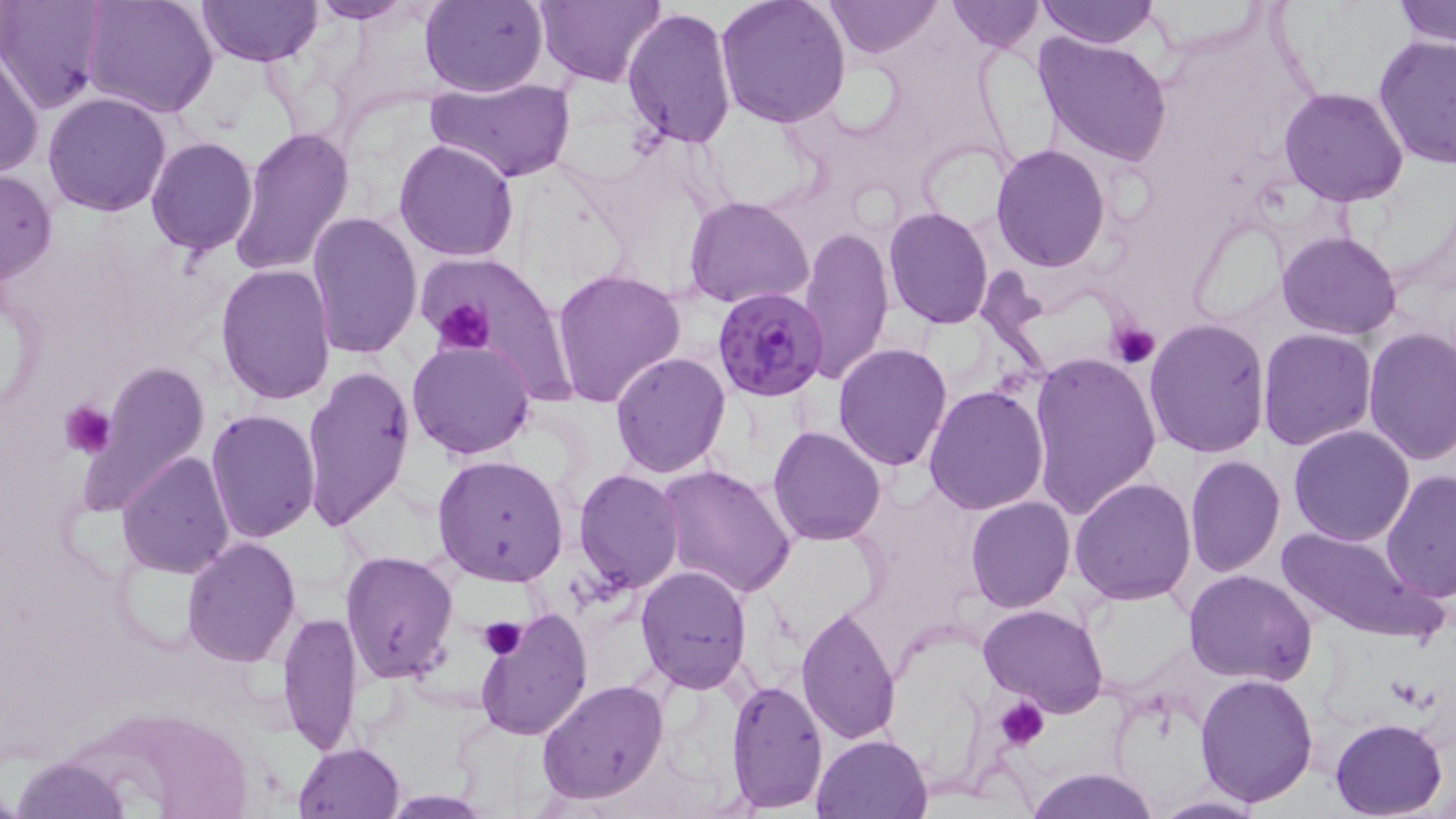
Summary:
  - Coordinate format: approximate bounding boxes as [x1, y1, x2, y2] in pixels
  - Uninfected red blood cell locations: [0, 0, 107, 112], [81, 0, 219, 118], [194, 0, 325, 67], [306, 0, 418, 22], [419, 0, 548, 98], [537, 0, 662, 87], [715, 0, 852, 128], [822, 0, 942, 57], [944, 0, 1045, 53], [1037, 0, 1160, 48], [1398, 0, 1456, 48], [622, 6, 737, 149], [1034, 31, 1172, 167], [1373, 34, 1456, 169], [0, 49, 44, 179], [427, 77, 573, 184], [1278, 87, 1409, 208], [43, 91, 171, 217], [229, 125, 354, 275], [145, 135, 259, 255], [394, 137, 521, 261], [991, 143, 1111, 270], [0, 169, 58, 287], [686, 196, 814, 310], [883, 208, 994, 330], [305, 210, 423, 359], [800, 225, 893, 383], [1278, 232, 1402, 340], [215, 263, 336, 406], [551, 268, 687, 407], [3, 279, 47, 419], [1143, 317, 1271, 458], [1258, 327, 1376, 449], [1362, 328, 1456, 466], [406, 338, 536, 461], [833, 343, 956, 469], [1027, 349, 1162, 517], [609, 351, 730, 476], [82, 358, 211, 512], [302, 362, 416, 533], [923, 384, 1051, 516], [205, 407, 320, 543], [767, 426, 887, 547], [1288, 426, 1415, 547], [117, 450, 236, 578], [432, 454, 569, 587], [1185, 454, 1285, 578], [656, 463, 798, 599], [574, 468, 683, 594], [1380, 471, 1456, 600], [1069, 478, 1197, 606], [964, 496, 1075, 613], [1276, 526, 1438, 644], [181, 536, 302, 666], [340, 550, 459, 685], [636, 567, 753, 694], [1183, 568, 1316, 684], [796, 603, 900, 745], [978, 603, 1109, 717], [278, 609, 366, 755], [474, 610, 593, 739], [1194, 672, 1318, 806], [536, 679, 669, 804], [727, 680, 827, 808], [1328, 717, 1448, 819], [811, 733, 932, 818], [293, 741, 405, 819], [10, 753, 130, 819], [1026, 767, 1160, 819], [1147, 795, 1266, 818]
  - Platelet locations: [428, 297, 496, 357], [1108, 320, 1161, 368], [59, 399, 116, 460], [478, 618, 528, 660], [996, 697, 1050, 749]
  - Plasmodium falciparum-infected red blood cell locations: [712, 286, 830, 401]
  - Slide-level diagnosis: Plasmodium falciparum
  - Stain: May-Grünwald-Giemsa
  - Preparation: thin blood smear
  - Image size: 1456×819 pixels
  - Modality: optical microscopy
  - Magnification: 1000x
  - Field of view: one of a larger specimen